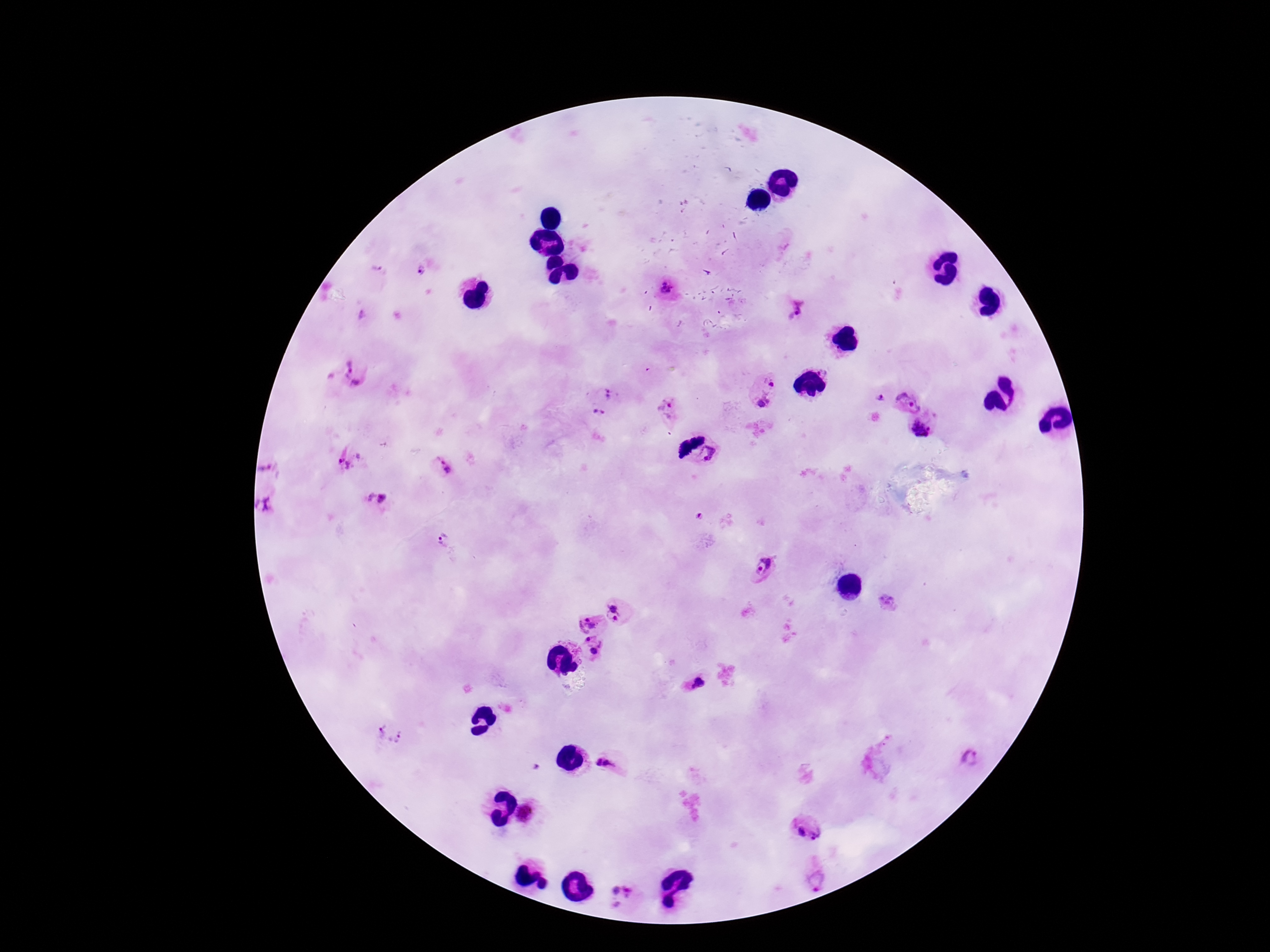
{
  "preparation": "thick blood smear",
  "magnification": "100x",
  "plasmodium_parasite_locations": "approximate centers as {x, y} in pixels: {377, 267}, {421, 271}, {667, 290}, {795, 310}, {362, 317}, {354, 375}, {330, 378}, {770, 379}, {609, 394}, {880, 397}, {762, 400}, {908, 402}, {666, 405}, {598, 412}, {921, 430}, {690, 448}, {711, 453}, {348, 458}, {441, 467}, {265, 469}, {369, 496}, {382, 498}, {264, 506}, {699, 516}, {443, 541}, {763, 568}, {887, 603}, {617, 613}, {588, 625}, {591, 649}, {693, 683}, {391, 734}, {968, 759}, {597, 761}, {609, 764}, {537, 767}, {525, 813}, {800, 832}, {817, 834}, {817, 877}, {624, 894}",
  "patient_malaria_status": "infected",
  "stain": "Giemsa",
  "capture": "smartphone camera through the microscope eyepiece",
  "field_of_view": "one from this slide",
  "image_size": "1270×952 pixels"
}